Assess for malaria.
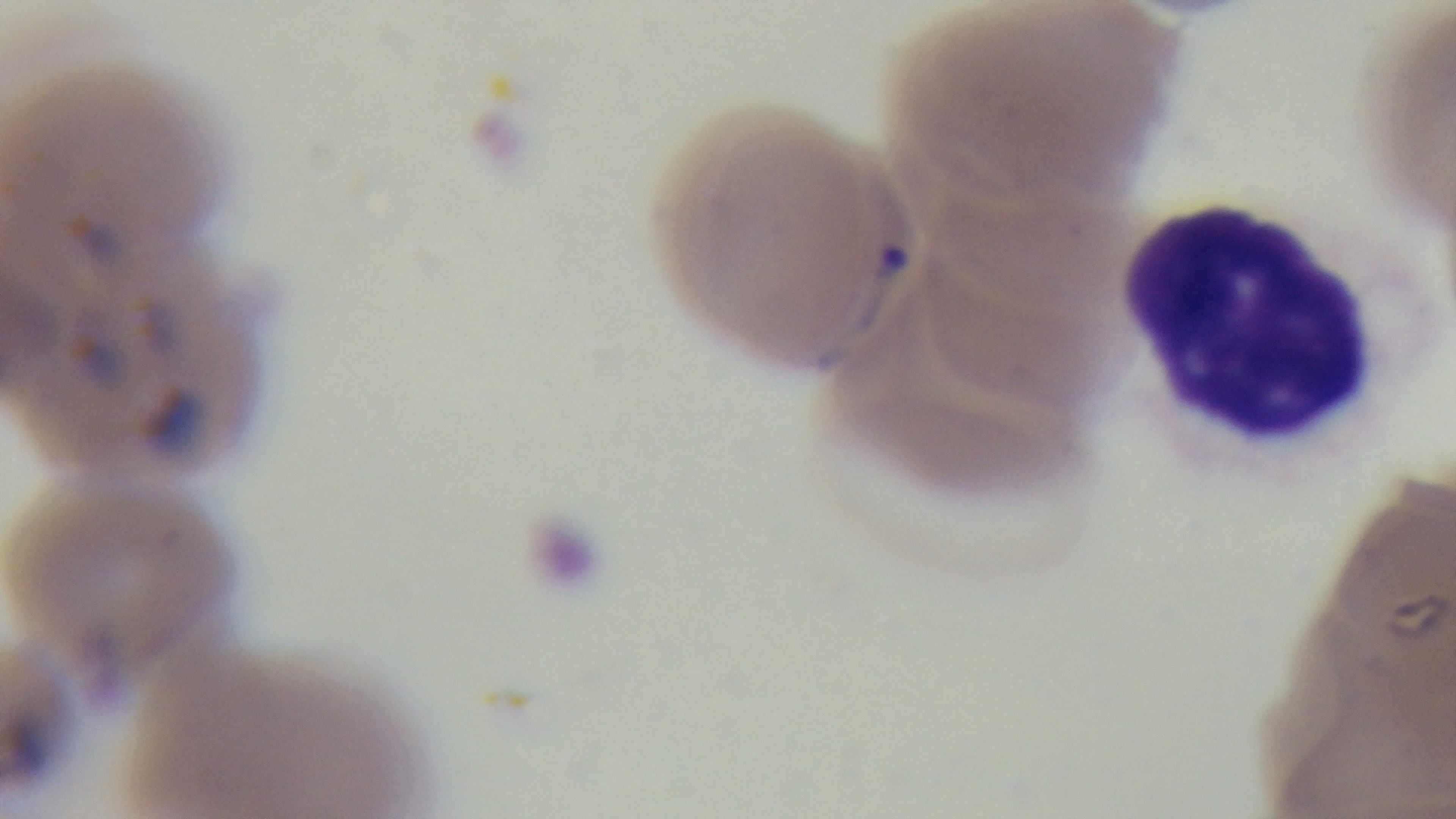
Positive.

Giemsa stain. One field from the slide. Preparation: thin smear. Light microscopy. Captured with a mounted 4K digital camera. Oil-immersion objective, 100x.